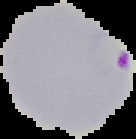

Summary:
  - Image type: cell region segmented out of the field of view; surrounding area masked to black
  - Image size: 136×139 pixels
  - Malaria status: parasitized
  - Preparation: thin blood film